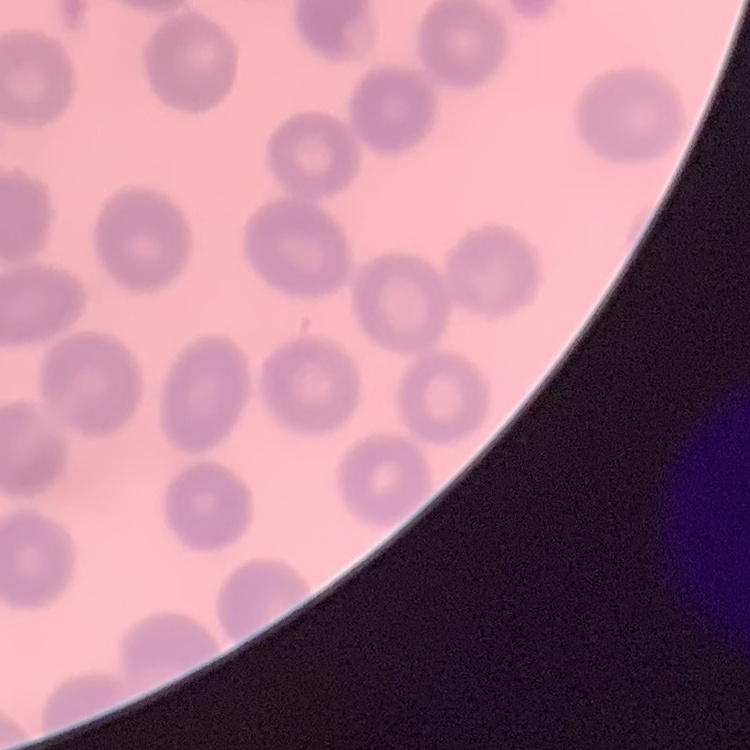

The erythrocytes show no rouleaux formation. Square crop of a larger photomicrograph. Thin blood film. Field's or Giemsa stain.